Locate and identify every blood parasite.
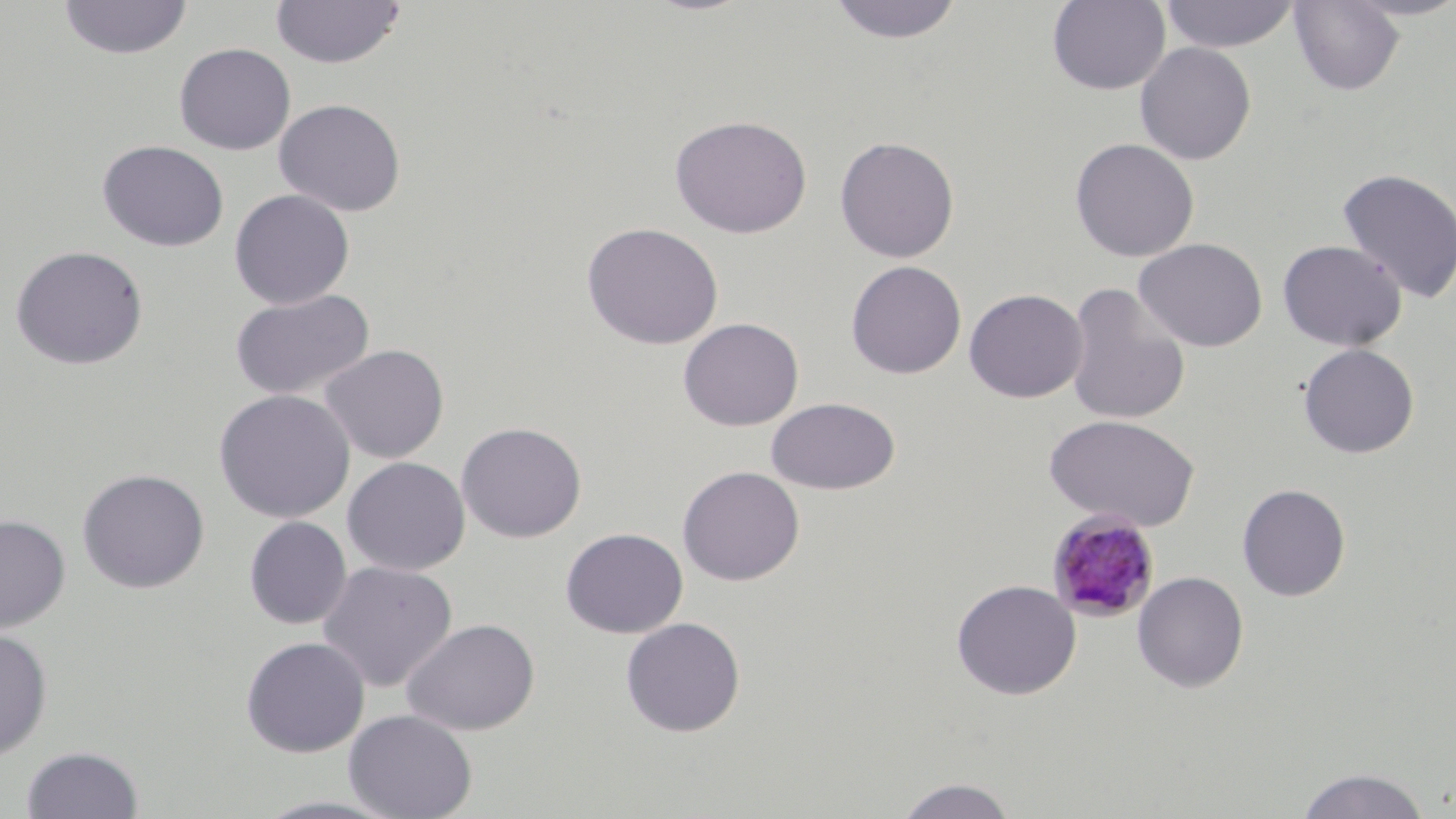

Approximate bounding boxes as (x1, y1, x2, y2) in pixels.
Plasmodium malariae-infected red blood cells: (1046, 508, 1161, 623).
No Plasmodium falciparum, Plasmodium ovale, Plasmodium vivax, Babesia divergens, or Trypanosoma brucei observed.

{
  "slide_level_diagnosis": "Plasmodium malariae",
  "magnification": "1000x",
  "modality": "optical microscopy",
  "image_size": "1456×819 pixels",
  "preparation": "thin blood smear",
  "field_of_view": "single",
  "uninfected_red_blood_cell_locations": "approximate bounding boxes as (x1, y1, x2, y2) in pixels: (58, 0, 193, 60), (271, 0, 406, 69), (827, 0, 966, 44), (1160, 0, 1300, 53), (1047, 1, 1170, 95), (1288, 1, 1405, 96), (1134, 42, 1257, 165), (174, 43, 296, 155), (273, 98, 407, 217), (670, 115, 812, 238), (834, 135, 960, 263), (1069, 137, 1200, 262), (97, 140, 229, 252), (1336, 167, 1456, 303), (229, 189, 355, 309), (581, 221, 723, 350), (1133, 237, 1268, 352), (1276, 239, 1407, 352), (10, 244, 149, 370), (846, 260, 967, 379), (1064, 282, 1192, 426), (964, 288, 1088, 402), (228, 289, 376, 401), (678, 317, 804, 431), (1298, 343, 1420, 458), (319, 344, 449, 463), (214, 389, 356, 523), (766, 396, 901, 495), (1043, 413, 1200, 531), (456, 421, 587, 543), (342, 457, 470, 575), (677, 465, 805, 586), (77, 468, 211, 594), (1236, 483, 1351, 602), (0, 514, 71, 633), (244, 516, 351, 629), (560, 527, 688, 638), (317, 560, 458, 692), (1132, 571, 1249, 693), (950, 579, 1082, 700), (621, 617, 746, 737), (402, 618, 540, 736), (0, 628, 54, 762), (240, 636, 370, 757), (344, 709, 478, 819), (21, 746, 144, 819), (1295, 767, 1433, 818), (893, 776, 1019, 818), (250, 795, 407, 818)",
  "stain": "May-Grünwald-Giemsa"
}